Classify this cell by malaria status.
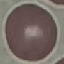
It is uninfected.

Giemsa stain. Automatically extracted cell patch, resized to 64 × 64 pixels. Acquired by smartphone through the microscope eyepiece. Thin blood film.